Classify this cell by malaria status.
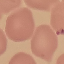
Uninfected.

capture: smartphone through the microscope eyepiece
preparation: thin smear
image_type: cell patch, automatically extracted from a larger field of view and resized to 64 × 64 pixels
stain: Giemsa